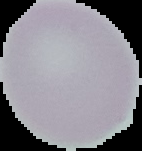

Image is 142×151 pixels. Malaria status: uninfected. From a thin blood film. Segmented cell region on a black background.